State the blood parasite species.
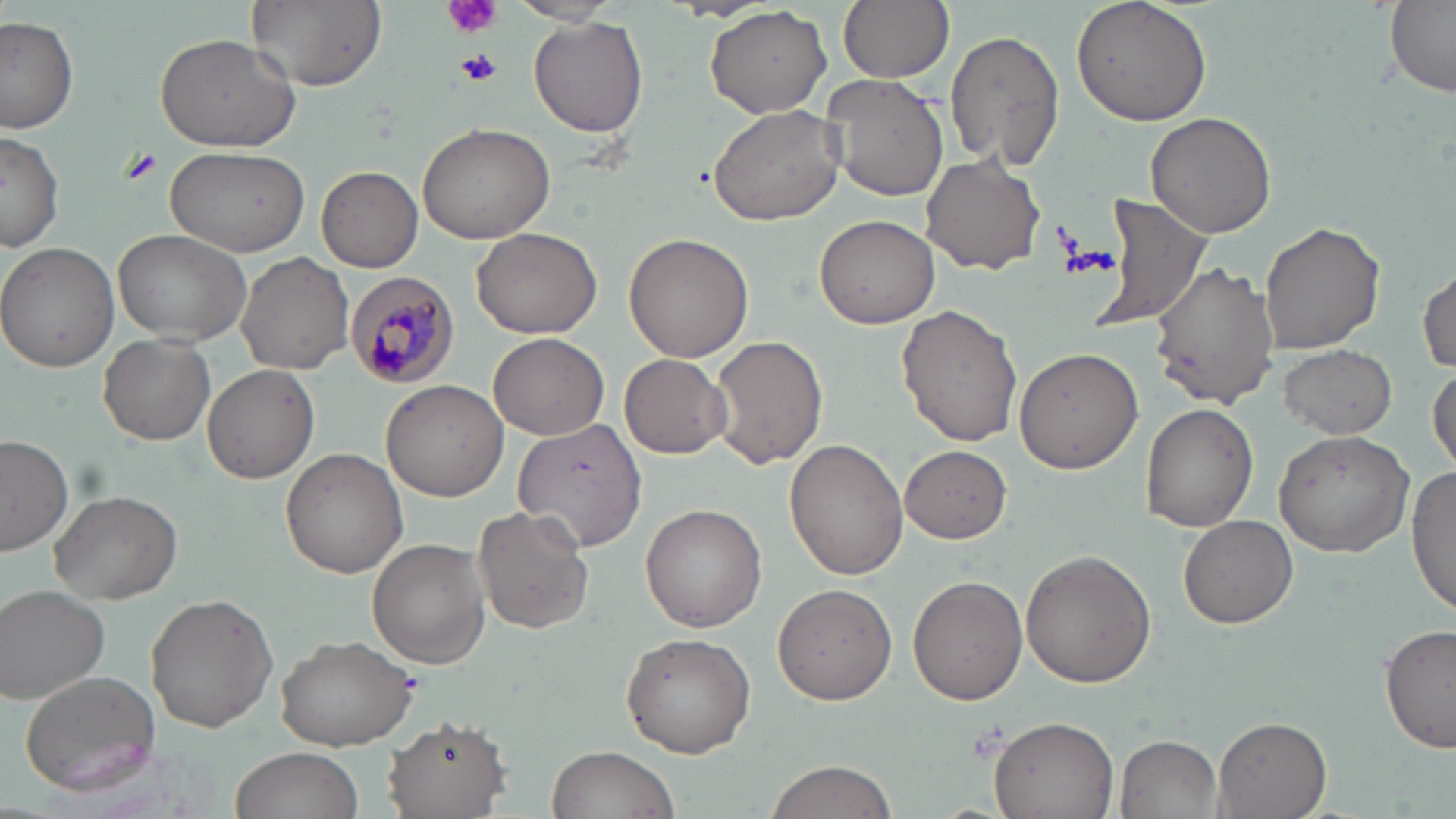
Plasmodium malariae.

Approximate bounding boxes as named x1/y1/x2/y2 corners in pixels. Uninfected red blood cell locations: (x1=246, y1=0, x2=387, y2=91), (x1=838, y1=0, x2=955, y2=84), (x1=1069, y1=0, x2=1212, y2=123), (x1=508, y1=1, x2=624, y2=27), (x1=1380, y1=2, x2=1456, y2=98), (x1=704, y1=6, x2=833, y2=118), (x1=0, y1=17, x2=78, y2=133), (x1=528, y1=18, x2=648, y2=138), (x1=945, y1=28, x2=1066, y2=173), (x1=154, y1=33, x2=300, y2=152), (x1=822, y1=75, x2=950, y2=203), (x1=707, y1=104, x2=846, y2=227), (x1=1145, y1=112, x2=1279, y2=240), (x1=418, y1=122, x2=556, y2=244), (x1=0, y1=127, x2=65, y2=254), (x1=166, y1=145, x2=310, y2=256), (x1=922, y1=155, x2=1047, y2=275), (x1=317, y1=166, x2=423, y2=272), (x1=1091, y1=195, x2=1212, y2=334), (x1=813, y1=213, x2=941, y2=330), (x1=1257, y1=219, x2=1386, y2=357), (x1=472, y1=227, x2=605, y2=340), (x1=114, y1=228, x2=252, y2=347), (x1=623, y1=233, x2=754, y2=362), (x1=0, y1=243, x2=121, y2=371), (x1=236, y1=250, x2=354, y2=374), (x1=1152, y1=261, x2=1281, y2=407), (x1=1416, y1=262, x2=1455, y2=374), (x1=895, y1=304, x2=1022, y2=447), (x1=489, y1=332, x2=609, y2=440), (x1=99, y1=333, x2=215, y2=444), (x1=710, y1=336, x2=828, y2=470), (x1=1280, y1=344, x2=1396, y2=438), (x1=1013, y1=347, x2=1143, y2=474), (x1=620, y1=354, x2=731, y2=458), (x1=202, y1=362, x2=320, y2=484), (x1=1429, y1=364, x2=1455, y2=474), (x1=382, y1=378, x2=511, y2=502), (x1=1140, y1=403, x2=1259, y2=532), (x1=512, y1=418, x2=646, y2=551), (x1=1273, y1=430, x2=1414, y2=557), (x1=0, y1=434, x2=74, y2=555), (x1=783, y1=438, x2=910, y2=582), (x1=900, y1=445, x2=1012, y2=543), (x1=281, y1=447, x2=410, y2=579), (x1=1407, y1=465, x2=1455, y2=620), (x1=49, y1=489, x2=181, y2=605), (x1=639, y1=503, x2=767, y2=631), (x1=473, y1=504, x2=594, y2=636), (x1=1178, y1=514, x2=1299, y2=628), (x1=367, y1=538, x2=490, y2=667), (x1=1019, y1=549, x2=1157, y2=687), (x1=910, y1=575, x2=1029, y2=704), (x1=772, y1=584, x2=897, y2=705), (x1=1, y1=586, x2=111, y2=703), (x1=146, y1=594, x2=278, y2=732), (x1=1381, y1=623, x2=1456, y2=758), (x1=619, y1=632, x2=755, y2=756), (x1=273, y1=633, x2=416, y2=749), (x1=19, y1=673, x2=160, y2=796), (x1=382, y1=714, x2=513, y2=817), (x1=988, y1=716, x2=1119, y2=818), (x1=1210, y1=717, x2=1332, y2=819), (x1=1115, y1=735, x2=1223, y2=818), (x1=546, y1=743, x2=681, y2=819), (x1=229, y1=747, x2=366, y2=819), (x1=763, y1=758, x2=898, y2=819). Plasmodium malariae-infected red blood cell locations: (x1=349, y1=270, x2=468, y2=387). Platelet locations: (x1=446, y1=0, x2=501, y2=38), (x1=455, y1=48, x2=502, y2=88), (x1=121, y1=148, x2=162, y2=185), (x1=964, y1=720, x2=1009, y2=763). May-Grünwald-Giemsa-stained preparation. Single field of view. Light microscopy. Captured at 1000x magnification. Thin blood film. Image is 1456×819 pixels.